Point out each Plasmodium parasite.
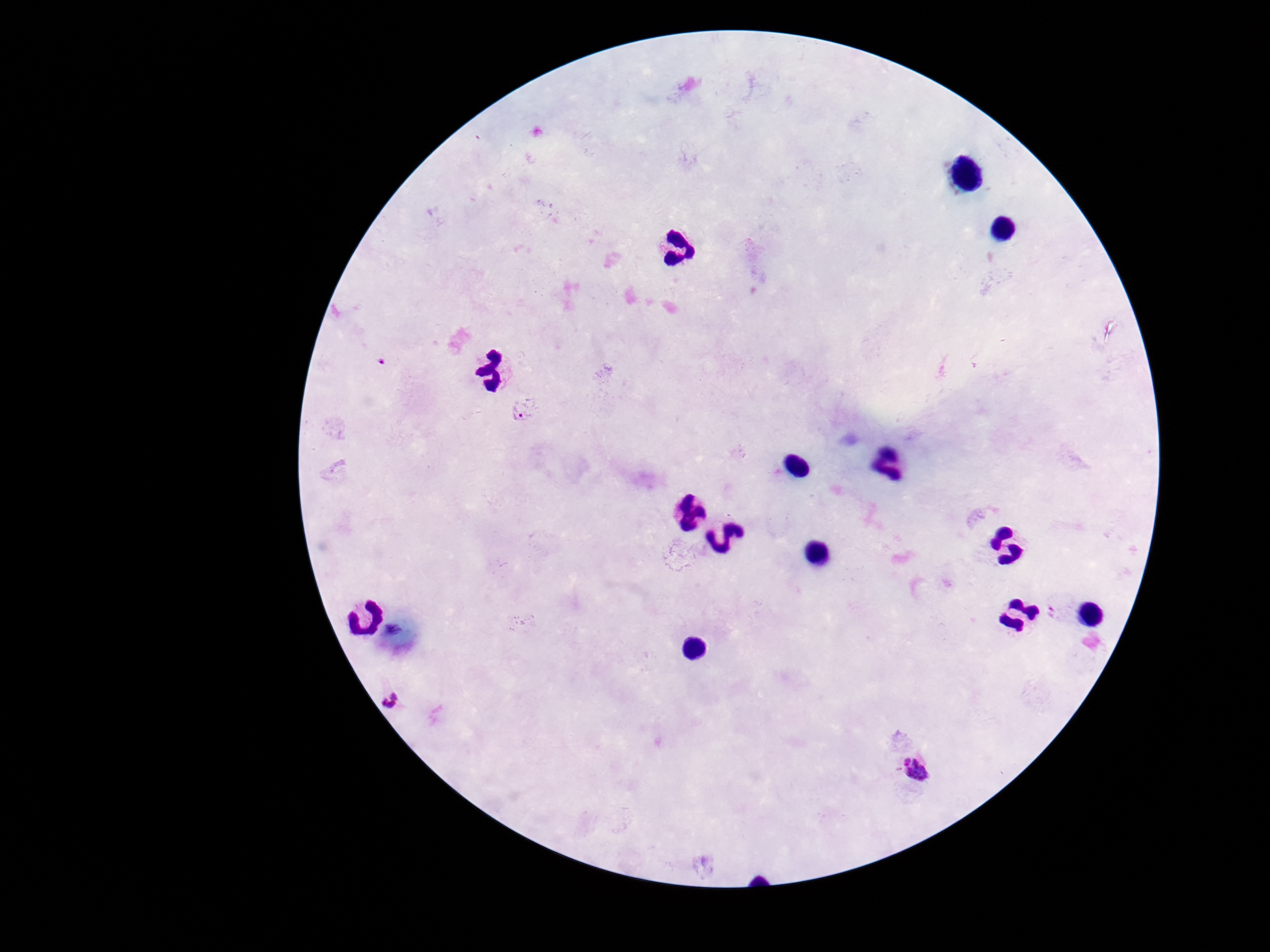

Approximate centers as {x, y} in pixels.
Plasmodium parasites: {523, 407}, {393, 696}, {918, 771}.

image size = 1270×952 pixels
preparation = thick blood film
magnification = 100x
capture = smartphone camera through the microscope eyepiece
patient malaria status = infected
stain = Giemsa
field of view = one from this slide